Classify this cell by malaria status.
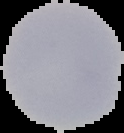

It is uninfected.

From a thin blood smear. Image is 124×133 pixels. Cell region segmented out of the field of view; the surrounding area is masked to black.